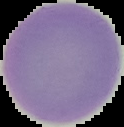

Summary:
  - Malaria status: uninfected
  - Image type: segmented cell region with the area outside set to black
  - Preparation: thin blood film
  - Image size: 124×127 pixels